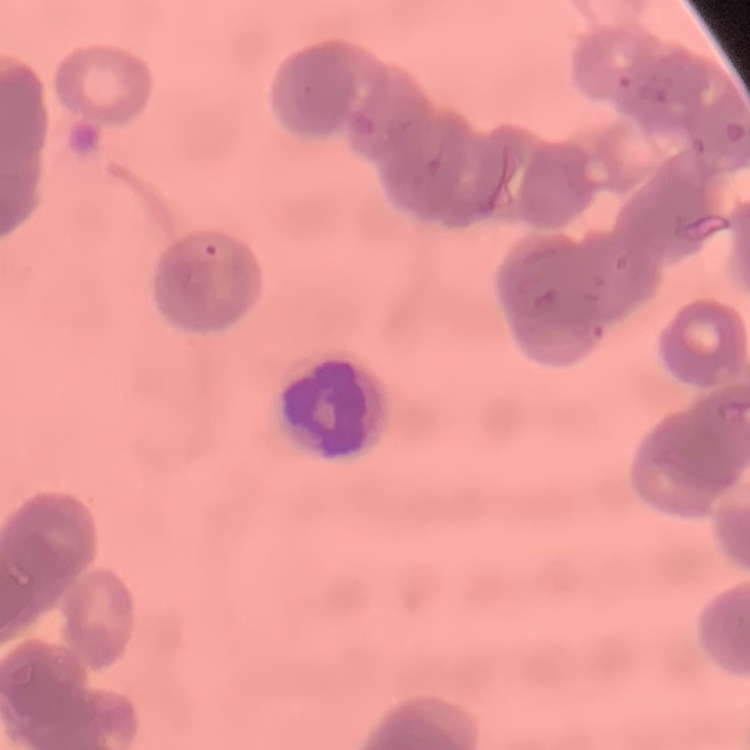

erythrocyte morphology = rouleaux formation
stain = Field's or Giemsa
image type = square crop of a larger photomicrograph
preparation = thin blood smear